Identify the cell.
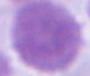
This is an erythrocyte.

1000x magnification. Photomicrograph.